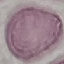

Summary:
  - Result: no malaria parasites detected
  - Capture: smartphone through the microscope eyepiece
  - Image type: cell patch, automatically extracted from a larger field of view and resized to 64 × 64 pixels
  - Stain: Giemsa
  - Preparation: thin smear